Identify the cell.
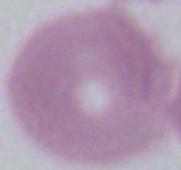

An erythrocyte.

magnification = 1000x
modality = photomicrograph